Assess this cell for malaria.
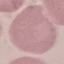
Uninfected.

stain = Giemsa
preparation = thin blood film
image type = cell patch, automatically extracted from a larger field of view and resized to 64 × 64 pixels
capture = smartphone through the microscope eyepiece